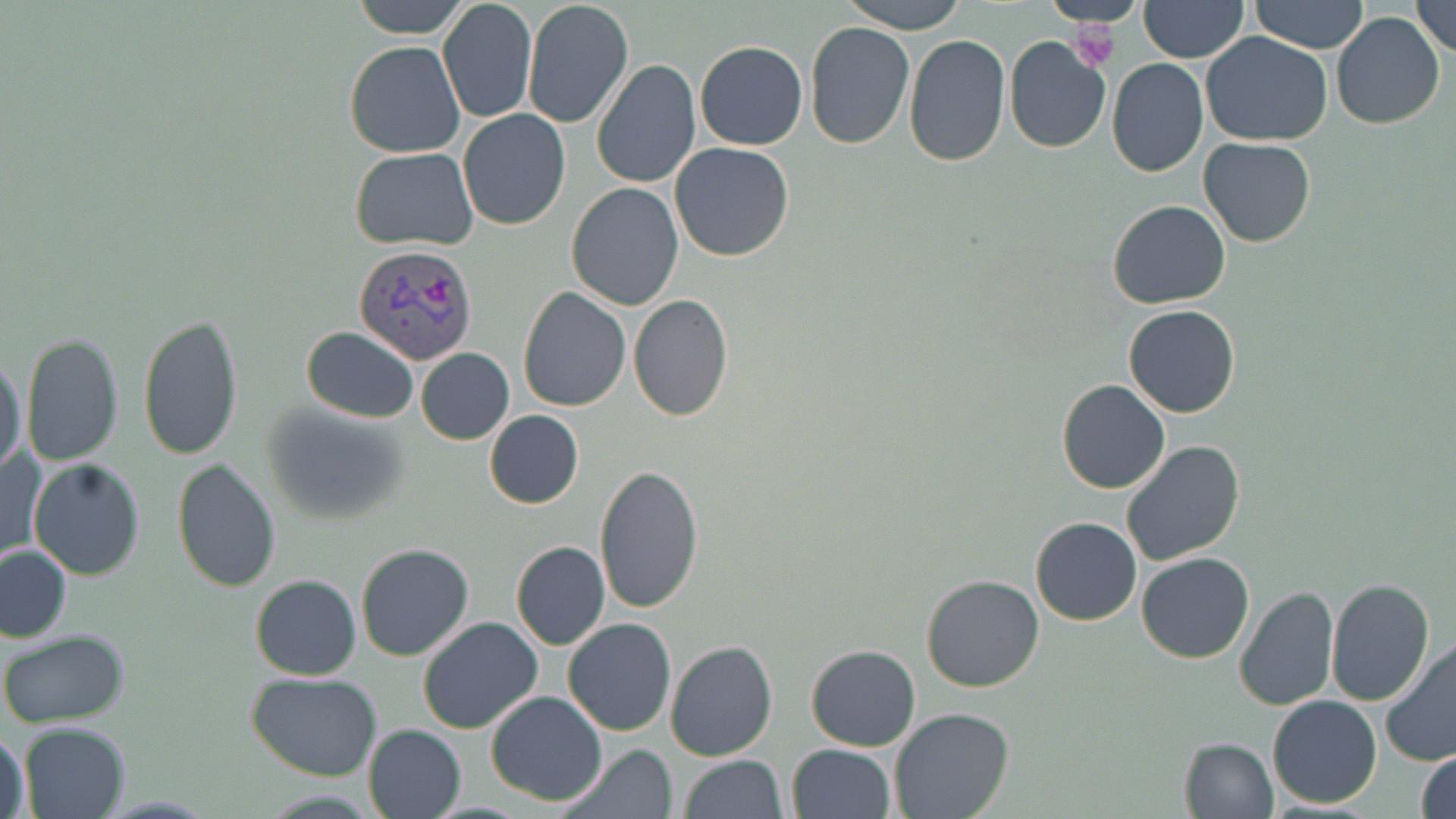

{
  "slide_level_diagnosis": "Plasmodium vivax",
  "field_of_view": "single",
  "image_size": "1456×819 pixels",
  "preparation": "thin blood film",
  "modality": "light microscopy",
  "magnification": "1000x",
  "stain": "May-Grünwald-Giemsa",
  "uninfected_red_blood_cell_locations": "approximate bounding boxes as (x1, y1, x2, y2) in pixels: (352, 0, 470, 39), (437, 0, 538, 124), (840, 0, 966, 32), (1043, 0, 1147, 28), (1139, 0, 1249, 63), (1250, 0, 1369, 53), (521, 1, 634, 130), (1411, 2, 1456, 60), (1330, 10, 1446, 131), (804, 22, 916, 150), (1201, 31, 1333, 146), (903, 35, 1010, 170), (1005, 38, 1112, 153), (345, 40, 465, 158), (695, 41, 808, 150), (1107, 58, 1207, 177), (591, 59, 701, 189), (458, 109, 571, 231), (1197, 136, 1316, 246), (669, 142, 796, 261), (351, 147, 477, 250), (566, 182, 684, 311), (1107, 200, 1231, 311), (518, 288, 631, 411), (628, 295, 733, 423), (1124, 304, 1241, 418), (136, 313, 243, 460), (301, 327, 418, 422), (21, 332, 125, 466), (416, 348, 514, 444), (0, 354, 26, 478), (1056, 379, 1171, 494), (260, 400, 413, 525), (483, 409, 583, 509), (1120, 440, 1247, 569), (2, 446, 44, 567), (28, 458, 146, 580), (171, 458, 281, 593), (594, 466, 704, 615), (1030, 516, 1142, 625), (511, 541, 610, 652), (355, 543, 474, 661), (2, 546, 71, 641), (1136, 551, 1254, 663), (920, 573, 1045, 693), (250, 574, 361, 680), (1325, 576, 1433, 706), (1233, 587, 1339, 712), (417, 616, 542, 734), (564, 618, 677, 737), (1, 630, 129, 727), (664, 641, 778, 762), (1381, 643, 1456, 769), (806, 644, 921, 751), (247, 671, 383, 781), (484, 692, 608, 806), (1267, 694, 1382, 808), (888, 708, 1015, 819), (19, 721, 131, 819), (362, 724, 466, 819), (2, 726, 29, 817), (1177, 736, 1279, 819), (787, 743, 896, 819), (561, 744, 677, 819), (1415, 749, 1456, 819), (679, 756, 787, 818)",
  "plasmodium_vivax_infected_red_blood_cell_locations": "approximate bounding boxes as (x1, y1, x2, y2) in pixels: (353, 245, 480, 364)",
  "platelet_locations": "approximate bounding boxes as (x1, y1, x2, y2) in pixels: (1070, 24, 1121, 70)"
}